Outline each blood parasite and name the species.
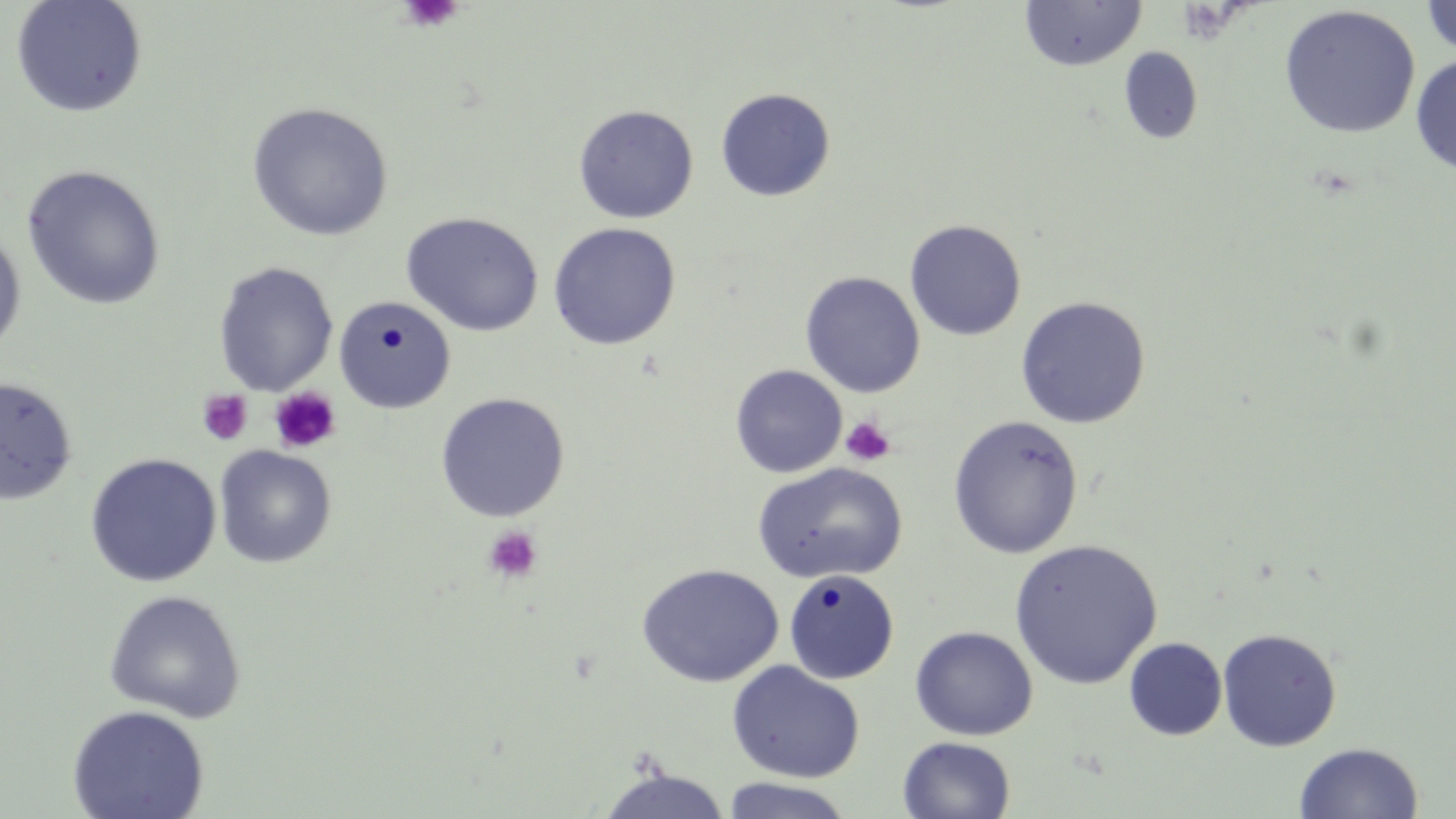
No blood parasites seen.

Approximate bounding boxes as (x1, y1, x2, y2) in pixels. Uninfected red blood cell locations: (10, 0, 148, 118), (1420, 0, 1456, 58), (1018, 1, 1146, 72), (1278, 5, 1421, 139), (1118, 47, 1203, 145), (1410, 53, 1456, 177), (715, 87, 836, 201), (246, 102, 394, 241), (573, 104, 699, 224), (21, 165, 167, 311), (400, 211, 544, 337), (904, 219, 1027, 341), (547, 222, 682, 350), (0, 228, 27, 358), (213, 261, 339, 396), (800, 271, 925, 398), (333, 295, 456, 414), (1015, 296, 1151, 428), (730, 364, 847, 478), (1, 376, 78, 506), (435, 391, 570, 522), (947, 415, 1085, 559), (214, 446, 337, 569), (85, 453, 222, 587), (752, 462, 907, 585), (1009, 538, 1163, 689), (636, 563, 784, 688), (783, 569, 900, 685), (104, 589, 247, 723), (910, 626, 1038, 740), (1218, 628, 1341, 752), (1124, 637, 1227, 740), (727, 661, 865, 783), (67, 704, 210, 819), (897, 736, 1016, 819), (1294, 741, 1424, 819), (595, 767, 733, 819), (719, 777, 856, 818). Platelet locations: (398, 0, 462, 33), (268, 387, 341, 454), (197, 388, 254, 445), (841, 417, 895, 466), (483, 525, 543, 583). Slide-level diagnosis: negative for blood parasites. May-Grünwald-Giemsa stain. Thin blood smear. Captured at 1000x magnification. One field of a larger specimen. Image is 1456×819 pixels. Optical microscopy.